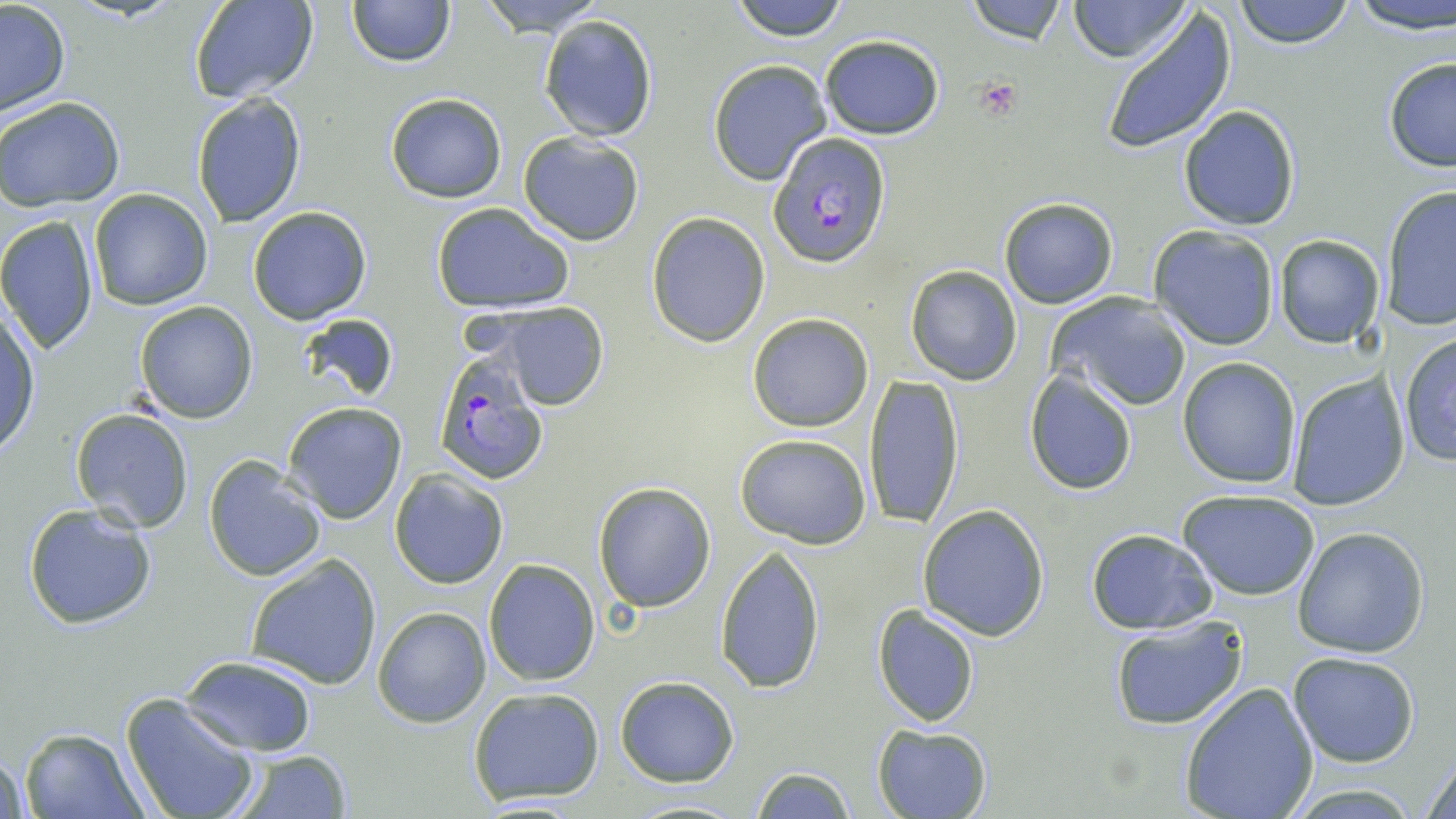

Approximate bounding boxes as (x1,y1)-(x2,y2) corner pairs in pixels. Platelet locations: (974,76)-(1024,118). Plasmodium falciparum-infected red blood cell locations: (768,136)-(885,267), (433,357)-(549,484). Uninfected red blood cell locations: (189,0)-(319,105), (349,0)-(454,67), (476,0)-(604,32), (728,0)-(852,40), (967,0)-(1068,45), (1069,0)-(1188,62), (1233,0)-(1354,49), (1348,0)-(1456,34), (0,3)-(71,117), (1098,8)-(1234,153), (538,15)-(658,142), (819,33)-(945,140), (1382,56)-(1456,172), (707,59)-(831,186), (191,93)-(307,228), (384,93)-(507,203), (2,97)-(125,209), (1178,105)-(1301,231), (517,131)-(645,245), (1381,186)-(1456,332), (90,190)-(213,311), (999,198)-(1118,310), (429,202)-(574,312), (247,205)-(372,324), (647,213)-(770,347), (0,217)-(99,357), (1148,225)-(1281,349), (1274,236)-(1385,349), (905,266)-(1023,385), (1049,293)-(1192,412), (135,301)-(257,422), (477,301)-(611,409), (295,311)-(400,403), (0,312)-(41,459), (746,313)-(875,431), (1400,333)-(1456,467), (1178,357)-(1302,489), (1024,370)-(1138,495), (1287,371)-(1409,511), (863,372)-(965,531), (284,401)-(408,524), (70,409)-(195,532), (735,433)-(872,549), (204,453)-(327,582), (389,469)-(508,588), (592,481)-(716,611), (1180,490)-(1320,600), (23,501)-(159,630), (918,504)-(1051,641), (1292,527)-(1429,657), (1086,529)-(1218,634), (715,544)-(825,694), (245,554)-(383,688), (483,559)-(600,687), (873,604)-(981,727), (372,606)-(491,728), (1108,616)-(1249,732), (1289,651)-(1421,768), (178,653)-(320,755), (615,676)-(739,786), (1178,681)-(1318,818), (467,687)-(606,805), (119,694)-(261,819), (872,724)-(991,818), (17,727)-(149,818), (1,745)-(29,819), (1423,745)-(1456,818), (227,748)-(352,818), (751,765)-(856,819), (621,797)-(750,818). Slide-level diagnosis: Plasmodium falciparum. Image is 1456×819 pixels. One field of a larger specimen. Captured at 1000x magnification. Thin blood film. May-Grünwald-Giemsa-stained preparation. Light microscopy.